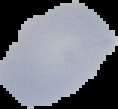

Segmented cell region on a black background. From a thin blood smear. Image is 118×109 pixels. Malaria status: uninfected.